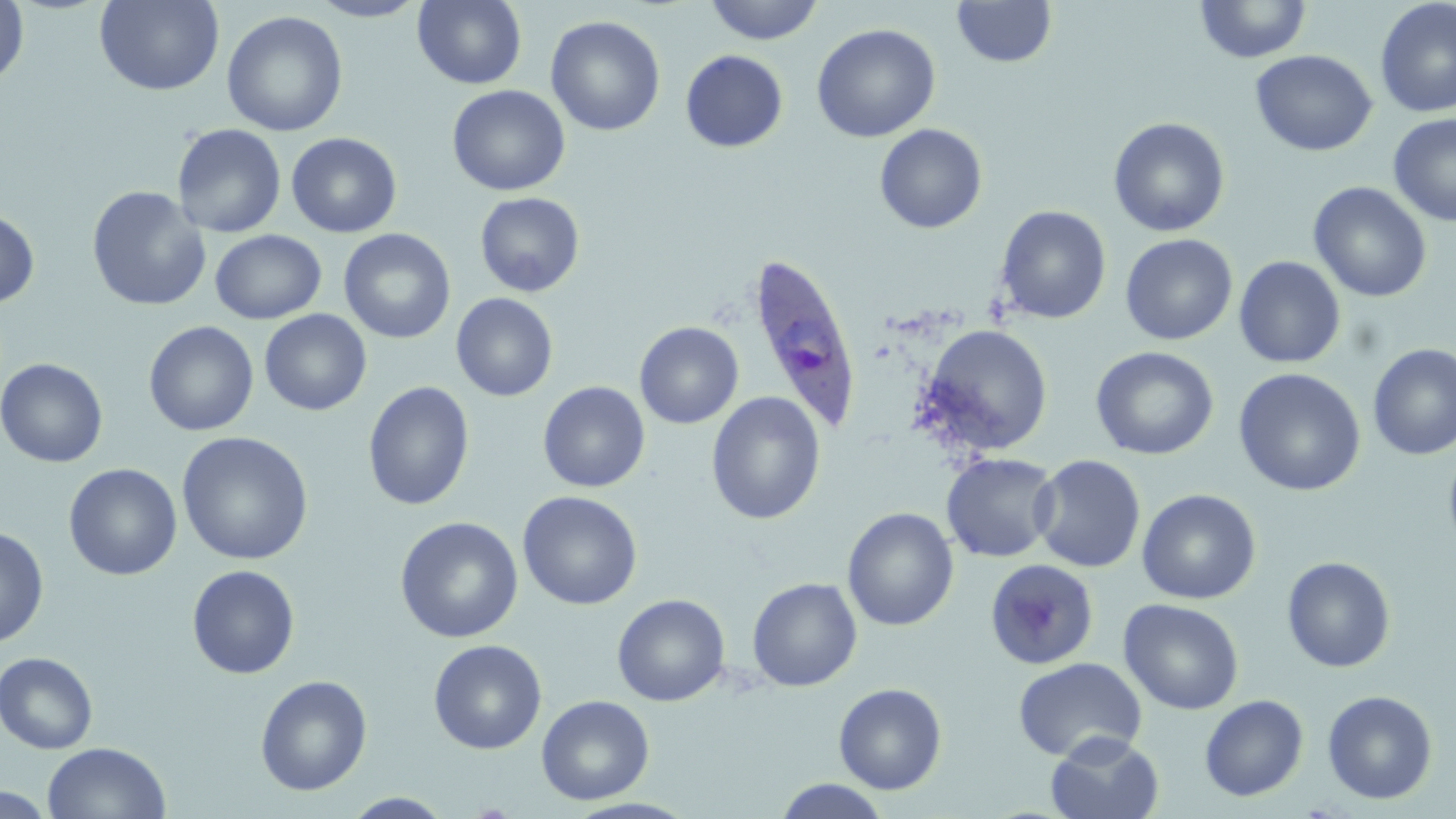

Approximate bounding boxes as named x1/y1/x2/y2 corners in pixels. Plasmodium ovale-infected red blood cell locations: (x1=745, y1=251, x2=864, y2=436). Uninfected red blood cell locations: (x1=0, y1=0, x2=30, y2=90), (x1=307, y1=0, x2=429, y2=22), (x1=412, y1=0, x2=527, y2=89), (x1=704, y1=0, x2=824, y2=45), (x1=1195, y1=0, x2=1312, y2=64), (x1=1375, y1=0, x2=1456, y2=118), (x1=93, y1=1, x2=225, y2=96), (x1=952, y1=1, x2=1057, y2=68), (x1=221, y1=10, x2=348, y2=137), (x1=546, y1=15, x2=666, y2=136), (x1=811, y1=23, x2=941, y2=143), (x1=680, y1=50, x2=788, y2=152), (x1=1250, y1=50, x2=1378, y2=157), (x1=447, y1=84, x2=570, y2=196), (x1=1388, y1=114, x2=1456, y2=226), (x1=1108, y1=117, x2=1230, y2=237), (x1=172, y1=123, x2=287, y2=237), (x1=874, y1=123, x2=988, y2=234), (x1=286, y1=132, x2=402, y2=238), (x1=1308, y1=181, x2=1432, y2=303), (x1=86, y1=186, x2=211, y2=311), (x1=474, y1=192, x2=585, y2=297), (x1=994, y1=205, x2=1112, y2=324), (x1=0, y1=209, x2=40, y2=309), (x1=338, y1=228, x2=456, y2=343), (x1=210, y1=230, x2=326, y2=324), (x1=1120, y1=233, x2=1238, y2=345), (x1=1234, y1=256, x2=1346, y2=369), (x1=451, y1=293, x2=558, y2=402), (x1=259, y1=309, x2=371, y2=415), (x1=143, y1=320, x2=259, y2=436), (x1=634, y1=322, x2=744, y2=429), (x1=919, y1=324, x2=1053, y2=454), (x1=1367, y1=343, x2=1456, y2=461), (x1=1090, y1=346, x2=1219, y2=460), (x1=1, y1=358, x2=108, y2=468), (x1=1233, y1=368, x2=1366, y2=496), (x1=362, y1=380, x2=475, y2=511), (x1=538, y1=381, x2=650, y2=492), (x1=706, y1=392, x2=826, y2=525), (x1=177, y1=432, x2=313, y2=565), (x1=1443, y1=440, x2=1456, y2=559), (x1=941, y1=453, x2=1061, y2=563), (x1=1030, y1=454, x2=1146, y2=572), (x1=63, y1=463, x2=183, y2=580), (x1=1137, y1=488, x2=1261, y2=605), (x1=517, y1=490, x2=642, y2=610), (x1=843, y1=507, x2=960, y2=631), (x1=395, y1=516, x2=523, y2=643), (x1=0, y1=525, x2=49, y2=648), (x1=1281, y1=556, x2=1396, y2=673), (x1=985, y1=559, x2=1099, y2=670), (x1=186, y1=564, x2=300, y2=680), (x1=747, y1=578, x2=862, y2=692), (x1=612, y1=594, x2=731, y2=706), (x1=1119, y1=598, x2=1244, y2=715), (x1=428, y1=639, x2=547, y2=755), (x1=0, y1=652, x2=98, y2=754), (x1=1013, y1=657, x2=1147, y2=763), (x1=255, y1=674, x2=372, y2=796), (x1=833, y1=682, x2=948, y2=795), (x1=1321, y1=690, x2=1438, y2=805), (x1=536, y1=695, x2=655, y2=805), (x1=1199, y1=695, x2=1309, y2=802), (x1=1046, y1=732, x2=1164, y2=819), (x1=41, y1=741, x2=172, y2=819), (x1=774, y1=779, x2=891, y2=818), (x1=0, y1=787, x2=56, y2=818), (x1=341, y1=791, x2=455, y2=817). Slide-level diagnosis: Plasmodium ovale. Optical microscopy. 1000x magnification. Single field of view. May-Grünwald-Giemsa-stained preparation. Image is 1456×819 pixels. Thin blood smear.